Mark where platelets are.
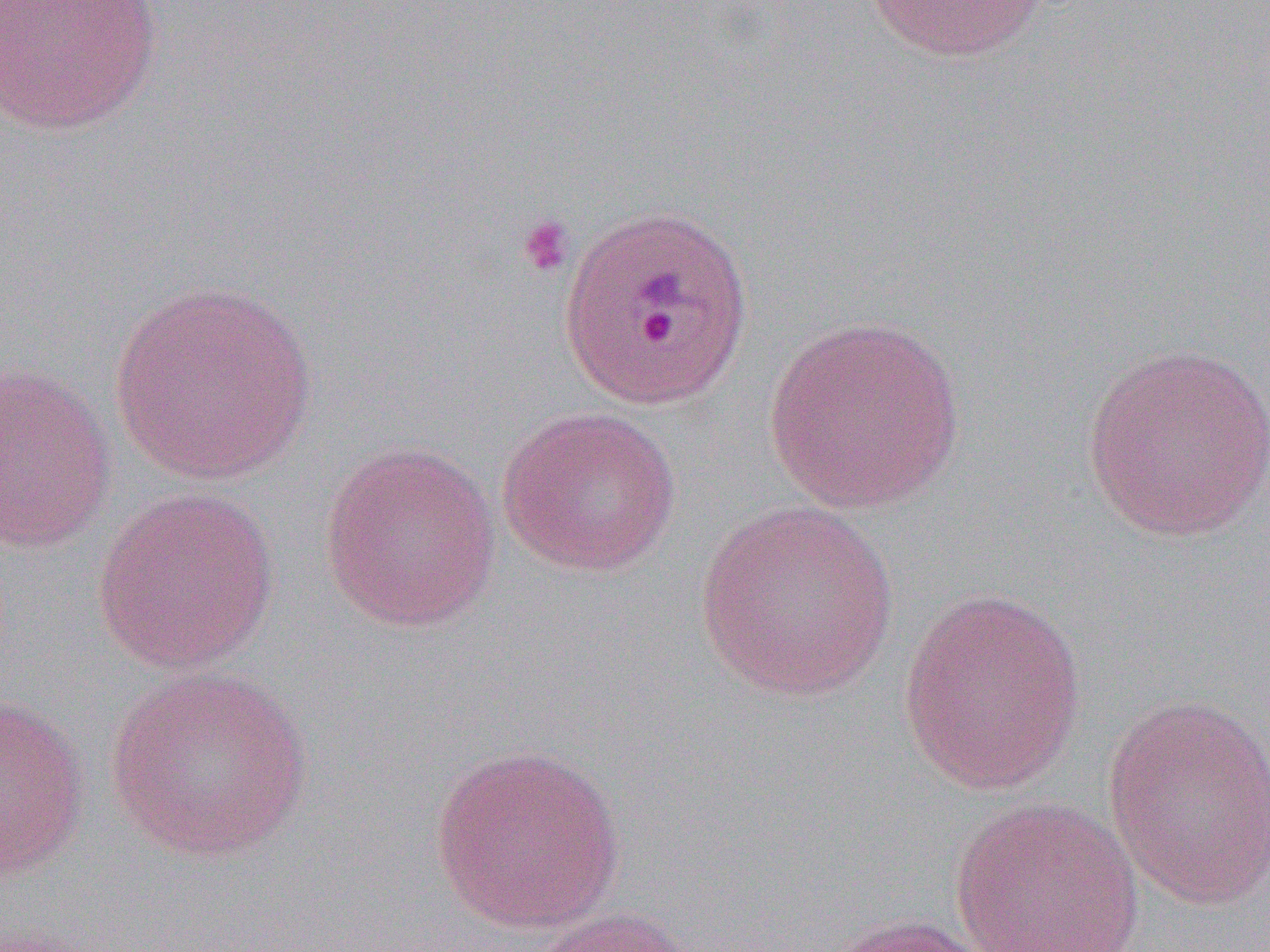
Approximate bounding boxes as named x1/y1/x2/y2 corners in pixels.
Platelets: (x1=514, y1=213, x2=575, y2=279).

Uninfected red blood cell locations: (x1=0, y1=0, x2=164, y2=136), (x1=864, y1=0, x2=1052, y2=63), (x1=560, y1=203, x2=754, y2=413), (x1=108, y1=277, x2=320, y2=485), (x1=763, y1=315, x2=968, y2=514), (x1=1080, y1=341, x2=1268, y2=544), (x1=0, y1=359, x2=117, y2=555), (x1=495, y1=405, x2=683, y2=577), (x1=318, y1=439, x2=502, y2=634), (x1=91, y1=487, x2=280, y2=675), (x1=693, y1=499, x2=901, y2=703), (x1=896, y1=585, x2=1088, y2=795), (x1=105, y1=665, x2=315, y2=863), (x1=0, y1=692, x2=91, y2=882), (x1=1101, y1=695, x2=1270, y2=910), (x1=429, y1=741, x2=626, y2=934), (x1=949, y1=797, x2=1145, y2=952), (x1=525, y1=906, x2=700, y2=952), (x1=821, y1=913, x2=1002, y2=952). Slide-level diagnosis: Plasmodium ovale. Captured at 1000x magnification. Thin blood smear. Optical microscopy. One field of a larger specimen. Image is 1270×952 pixels.